Classify this cell by malaria status.
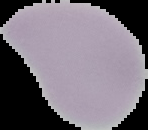
It is uninfected.

preparation = thin blood smear
image type = segmented cell region on a black background
image size = 148×130 pixels